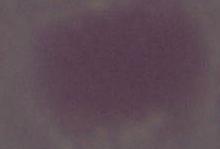
modality = micrograph
magnification = 1000x
identification = erythrocyte